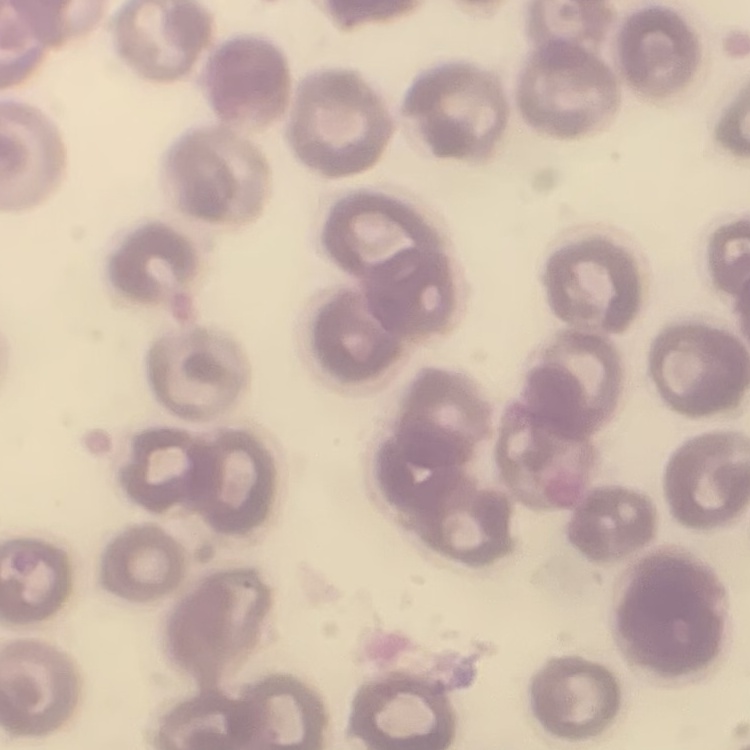
Summary:
  - Erythrocyte morphology: no rouleaux formation
  - Image type: one tile cut from a larger photomicrograph
  - Preparation: thin peripheral smear
  - Stain: Field's or Giemsa